Locate every blood parasite and identify its species.
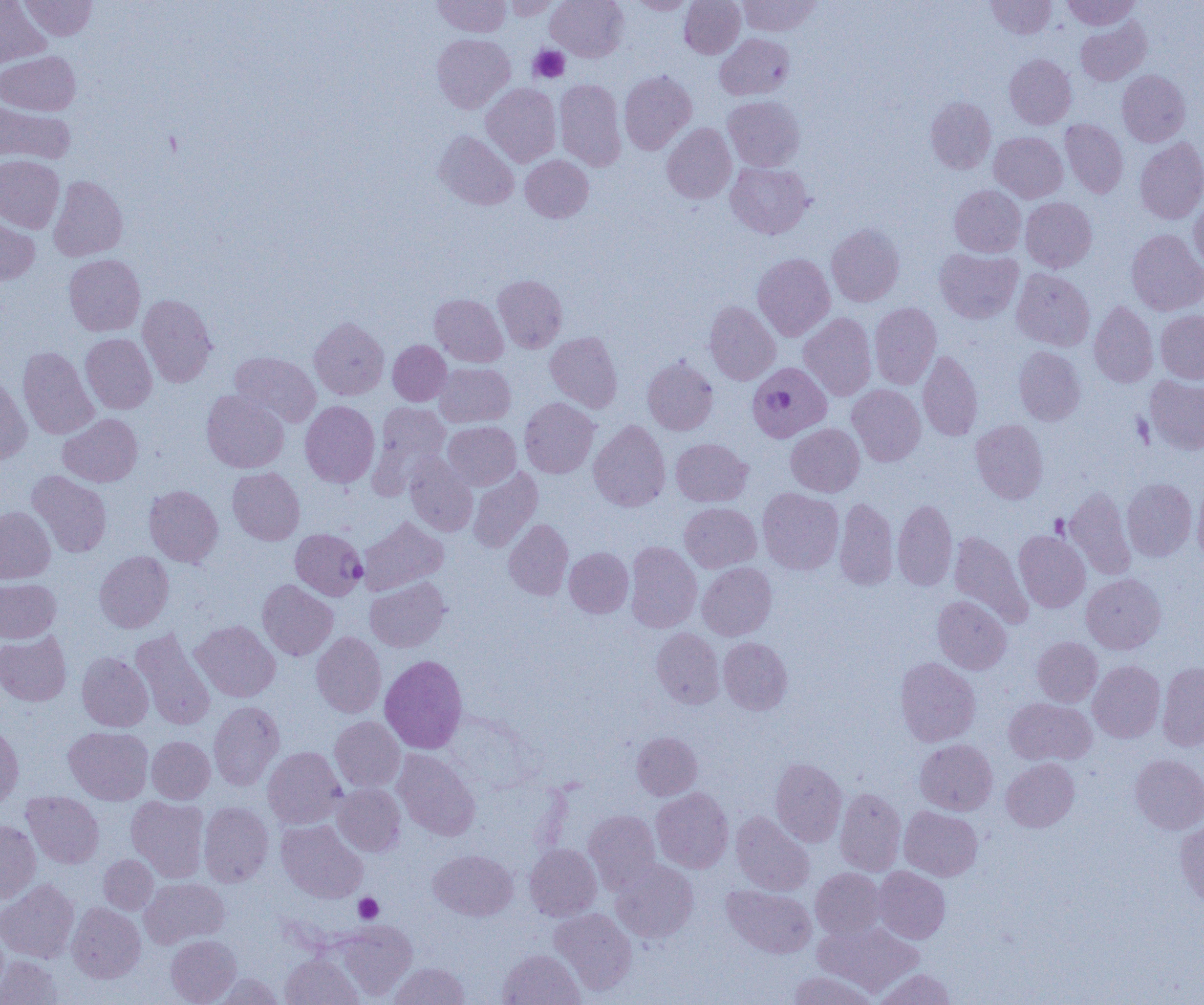

Approximate bounding boxes as [x1, y1, x2, y2] in pixels.
Plasmodium falciparum-infected red blood cells: [747, 362, 831, 442], [290, 528, 367, 600].
No Plasmodium ovale, Plasmodium malariae, Plasmodium vivax, Babesia divergens, or Trypanosoma brucei observed.

Summary:
  - Uninfected red blood cell locations: [20, 0, 98, 40], [432, 0, 511, 37], [503, 0, 563, 20], [545, 0, 628, 61], [628, 0, 697, 14], [679, 0, 745, 58], [738, 0, 823, 36], [986, 0, 1056, 39], [1061, 0, 1140, 30], [0, 1, 50, 69], [1074, 17, 1151, 86], [716, 33, 794, 100], [432, 34, 514, 113], [0, 51, 80, 115], [1005, 54, 1077, 129], [619, 70, 696, 154], [1117, 70, 1190, 146], [555, 79, 626, 171], [481, 83, 561, 167], [723, 96, 805, 171], [925, 96, 996, 174], [0, 100, 75, 165], [1060, 119, 1128, 198], [662, 123, 736, 204], [434, 130, 519, 210], [989, 132, 1068, 202], [1135, 138, 1204, 224], [0, 155, 64, 233], [520, 155, 594, 222], [725, 162, 814, 238], [48, 176, 127, 261], [949, 185, 1025, 257], [1020, 197, 1097, 272], [1189, 198, 1204, 274], [0, 212, 40, 285], [826, 223, 905, 306], [1126, 229, 1204, 315], [934, 248, 1023, 323], [752, 253, 835, 340], [63, 254, 145, 336], [1011, 268, 1095, 351], [493, 275, 567, 352], [430, 293, 508, 367], [137, 294, 217, 386], [704, 301, 780, 385], [1089, 301, 1158, 387], [869, 302, 941, 389], [1156, 310, 1204, 382], [799, 312, 876, 400], [309, 317, 389, 400], [545, 331, 622, 412], [80, 333, 157, 414], [388, 340, 451, 406], [17, 346, 98, 440], [1014, 346, 1086, 425], [918, 350, 982, 440], [230, 351, 321, 427], [642, 357, 718, 435], [434, 362, 515, 428], [0, 371, 32, 463], [1144, 375, 1204, 455], [847, 384, 926, 466], [201, 389, 289, 473], [519, 397, 599, 478], [300, 401, 380, 487], [368, 402, 451, 495], [58, 413, 143, 487], [971, 419, 1048, 504], [589, 420, 670, 512], [443, 421, 520, 490], [786, 423, 864, 496], [671, 438, 752, 507], [404, 453, 478, 536], [227, 467, 305, 545], [468, 467, 542, 553], [27, 470, 112, 557], [1122, 478, 1197, 560], [1193, 484, 1204, 567], [144, 485, 223, 567], [1064, 487, 1135, 578], [757, 488, 844, 575], [834, 497, 898, 591], [892, 499, 957, 591], [680, 502, 761, 572], [0, 506, 55, 584], [358, 516, 448, 595], [504, 519, 573, 600], [1014, 530, 1090, 612], [949, 531, 1032, 626], [625, 541, 701, 632], [564, 547, 633, 617], [95, 551, 173, 633], [697, 562, 777, 640], [1081, 573, 1166, 654], [365, 577, 450, 652], [0, 578, 60, 642], [257, 579, 338, 660], [933, 595, 1011, 674], [190, 620, 280, 701], [131, 628, 215, 730], [652, 628, 724, 708], [311, 632, 386, 718], [0, 633, 71, 706], [718, 637, 792, 715], [1032, 637, 1102, 706], [76, 652, 153, 731], [380, 655, 467, 753], [895, 657, 980, 746], [1088, 660, 1165, 743], [1157, 662, 1204, 751], [1003, 697, 1096, 766], [209, 700, 284, 790], [330, 716, 405, 792], [0, 722, 23, 808], [64, 726, 153, 804], [631, 732, 702, 800], [147, 736, 215, 803], [915, 739, 997, 815], [263, 746, 346, 828], [393, 749, 481, 840], [914, 750, 1078, 818], [1130, 754, 1204, 835], [770, 758, 847, 846], [1001, 758, 1079, 832], [333, 783, 405, 856], [651, 787, 733, 873], [835, 788, 906, 875], [22, 791, 104, 868], [126, 796, 210, 882], [199, 802, 273, 886], [899, 805, 982, 880], [584, 809, 660, 892], [731, 811, 814, 895], [1176, 818, 1204, 909], [0, 819, 40, 903], [276, 820, 367, 903], [524, 844, 601, 920], [428, 849, 517, 921], [98, 854, 158, 914], [611, 861, 698, 942], [873, 866, 950, 943], [811, 867, 886, 939], [140, 878, 229, 948], [0, 880, 79, 963], [722, 885, 816, 958], [67, 902, 145, 982], [549, 908, 637, 994], [334, 920, 417, 1000], [813, 920, 924, 997], [166, 935, 241, 1004], [497, 949, 585, 1005], [280, 954, 363, 1005], [0, 955, 63, 1005], [390, 962, 470, 1005], [874, 969, 956, 1005], [787, 971, 878, 1005], [212, 973, 283, 1004]
  - Platelet locations: [529, 46, 569, 83], [354, 893, 383, 923]
  - Slide-level diagnosis: Plasmodium falciparum
  - Image size: 1204×1005 pixels
  - Magnification: 1000x
  - Modality: optical microscopy
  - Preparation: thin blood smear
  - Field of view: single